Assess this cell for malaria.
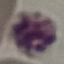

It is uninfected.

{
  "preparation": "thin blood smear",
  "image_type": "cell patch, automatically extracted from a larger field of view and resized to 64 × 64 pixels",
  "capture": "smartphone camera at the microscope eyepiece",
  "stain": "Giemsa"
}